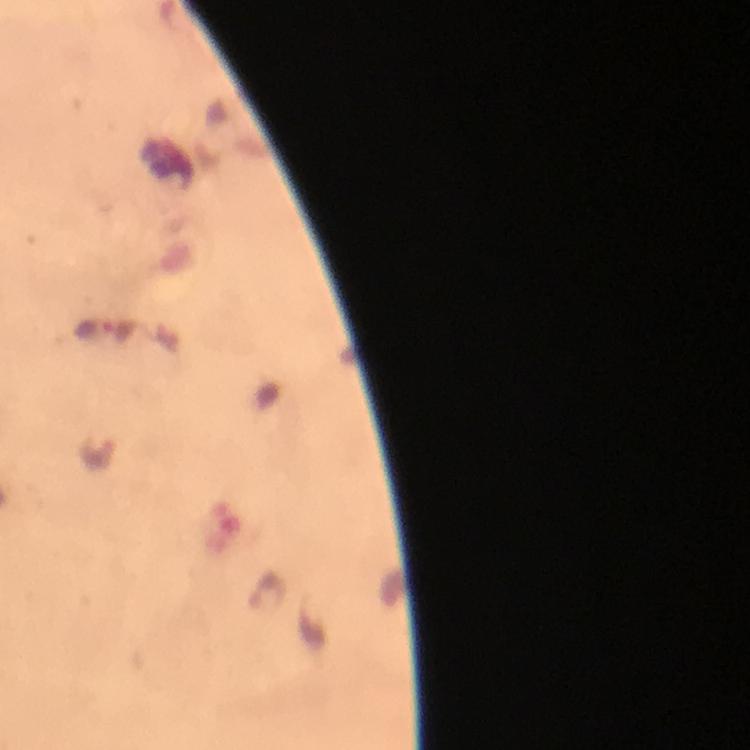

{
  "cropped_from": "a single field of view",
  "context": "from a diagnostic examination for malaria",
  "image_size": "750×750 pixels",
  "stain": "Giemsa",
  "capture": "smartphone photograph through a microscope",
  "magnification": "100x",
  "immersion_oil": "used",
  "preparation": "thick blood film",
  "malaria_parasite_locations": "approximate centers as [x, y] in pixels: [92, 329], [268, 592]"
}